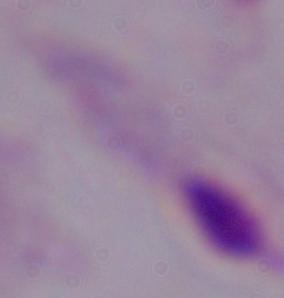
A trichomonad is seen. Captured at 1000x magnification. Photomicrograph.